Identify the preparation type.
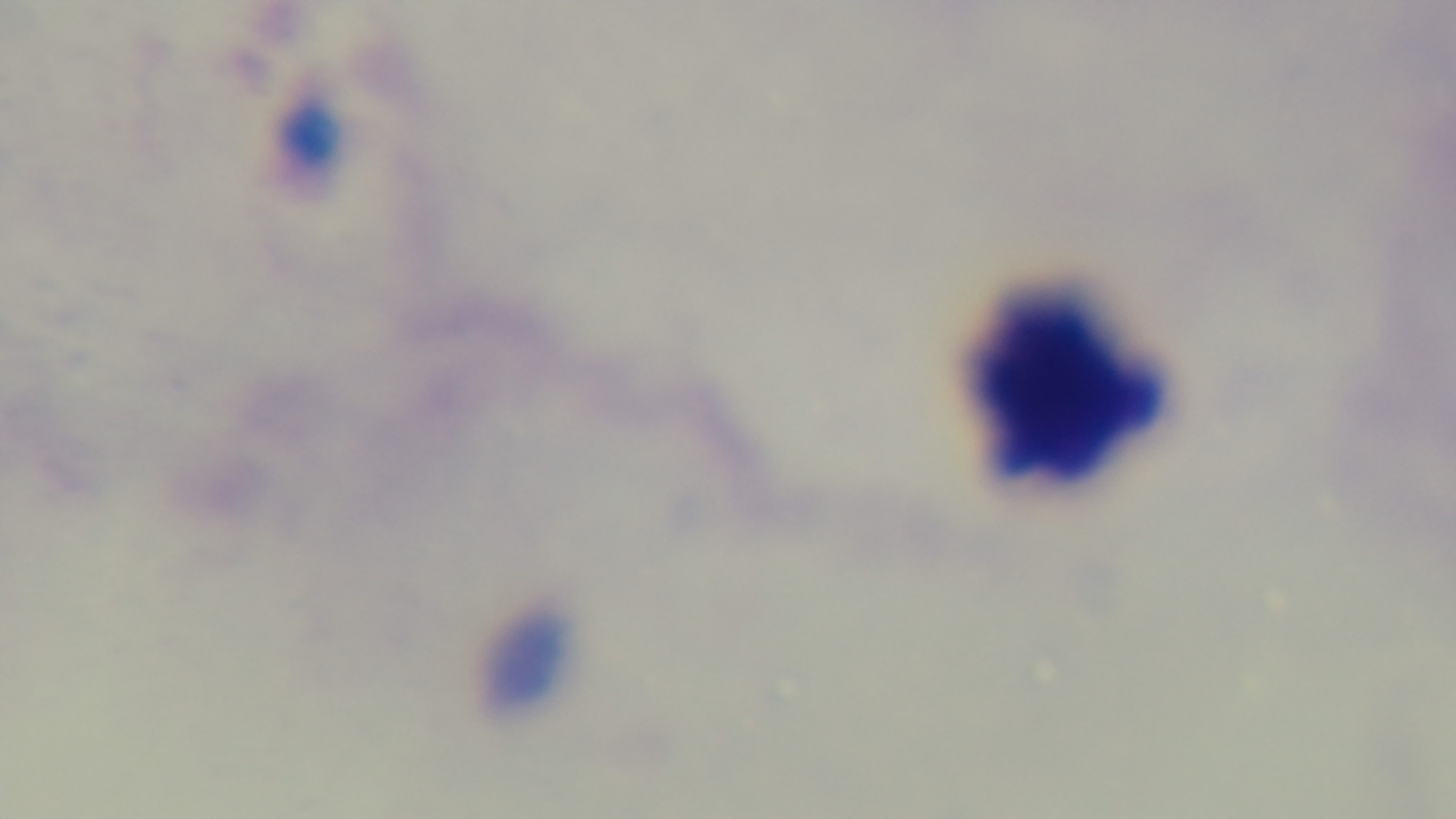
A thick smear.

Summary:
  - Objective: 100x oil immersion
  - Capture: mounted 4K digital camera
  - Malaria status: negative
  - Stain: Giemsa
  - Modality: light microscopy
  - Field of view: one from the slide